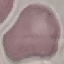

Summary:
  - Malaria status: uninfected
  - Preparation: thin smear
  - Stain: Giemsa
  - Image type: cell patch, automatically extracted from a larger field of view and resized to 64 × 64 pixels
  - Capture: smartphone camera at the microscope eyepiece